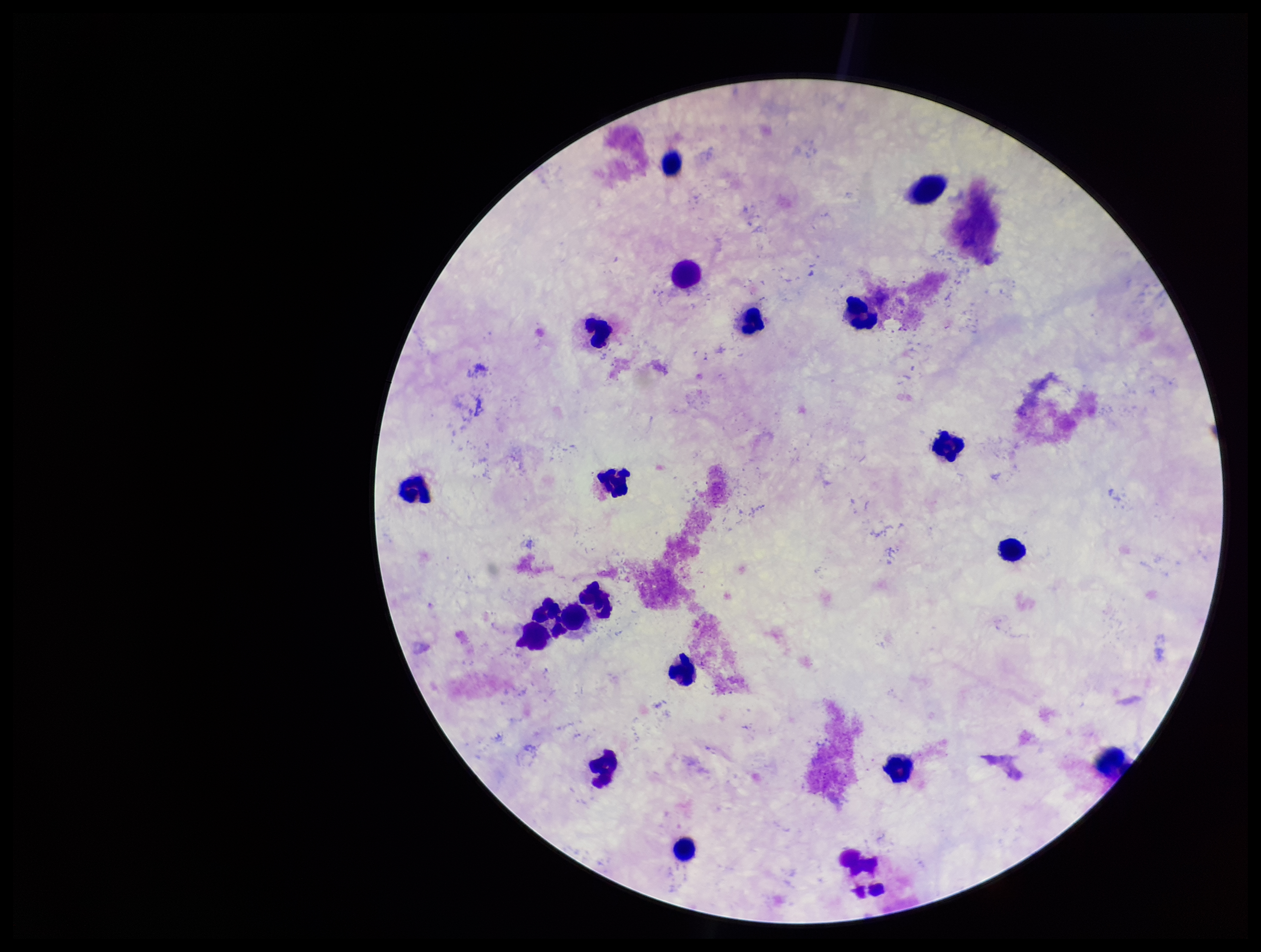
Single field of view. Patient malaria status: negative. Image is 1261×952 pixels. Plasmodium parasites: none detected. Preparation: thick. Smartphone photograph taken through the eyepiece of a microscope. Leukocyte count: 18. Parasite count: 0. Stained with Giemsa.